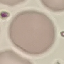

malaria status = uninfected
image type = cell patch, automatically extracted from a larger field of view and resized to 64 × 64 pixels
preparation = thin smear
stain = Giemsa
capture = smartphone camera at the microscope eyepiece